Assess this cell for malaria.
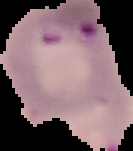

Parasitized.

Segmented cell region on a black background. From a thin blood film. Image is 133×151 pixels.